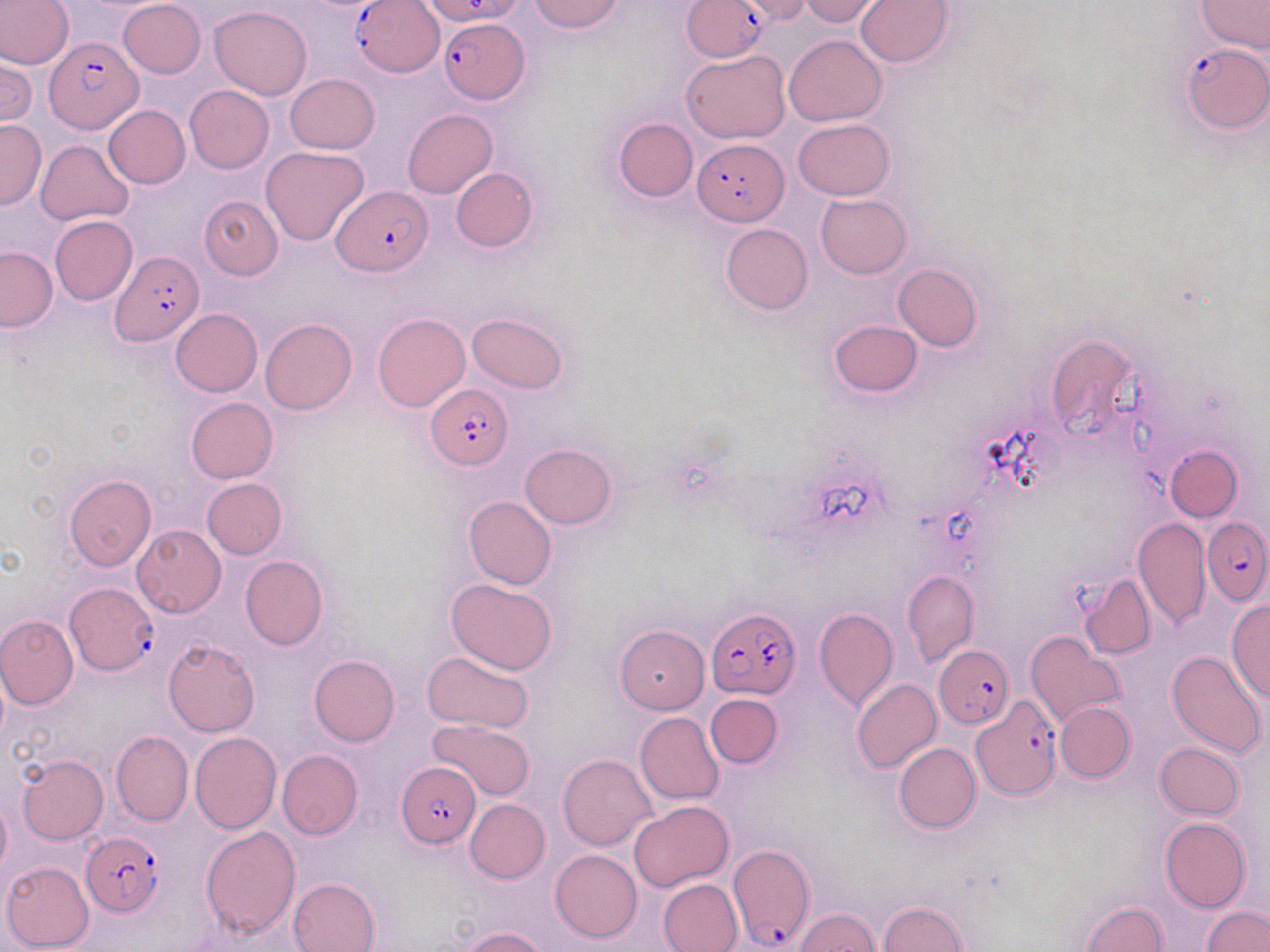
Summary:
  - Coordinate format: approximate bounding boxes as [x1, y1, x2, y2] in pixels
  - Uninfected red blood cell locations: [0, 0, 74, 70], [528, 0, 626, 34], [733, 0, 813, 23], [800, 0, 881, 25], [1196, 0, 1270, 55], [118, 1, 206, 79], [856, 1, 954, 68], [209, 6, 312, 100], [784, 35, 886, 126], [1, 50, 36, 129], [682, 50, 792, 144], [284, 74, 379, 154], [185, 85, 274, 174], [104, 105, 190, 189], [402, 109, 497, 198], [613, 117, 697, 201], [792, 118, 895, 200], [0, 119, 45, 210], [35, 139, 135, 226], [260, 145, 370, 247], [451, 167, 537, 252], [815, 194, 911, 278], [200, 196, 283, 280], [49, 214, 139, 305], [720, 223, 812, 315], [0, 246, 58, 332], [894, 263, 983, 352], [171, 308, 263, 397], [373, 312, 470, 411], [467, 312, 569, 393], [260, 318, 357, 415], [828, 320, 923, 398], [1043, 332, 1143, 442], [185, 397, 279, 483], [520, 443, 616, 529], [1165, 444, 1243, 521], [65, 475, 157, 570], [200, 478, 287, 560], [463, 495, 556, 590], [1133, 516, 1210, 631], [133, 524, 226, 618], [240, 555, 329, 649], [902, 570, 979, 666], [1079, 573, 1157, 659], [446, 578, 558, 675], [1226, 601, 1270, 703], [813, 607, 898, 711], [0, 615, 79, 709], [615, 624, 711, 714], [1024, 633, 1124, 729], [163, 638, 259, 735], [1167, 649, 1267, 758], [422, 650, 536, 736], [309, 654, 400, 747], [851, 678, 942, 773], [706, 693, 782, 767], [1055, 700, 1134, 783], [635, 712, 725, 804], [428, 719, 537, 801], [112, 730, 193, 826], [190, 732, 281, 833], [893, 742, 982, 833], [1154, 743, 1245, 820], [277, 749, 363, 840], [17, 753, 108, 844], [558, 753, 657, 852], [0, 796, 11, 879], [464, 799, 550, 883], [629, 800, 732, 891], [1160, 817, 1251, 913], [199, 824, 300, 938], [550, 850, 643, 942], [2, 861, 95, 950], [287, 877, 381, 952], [658, 878, 744, 952], [878, 901, 968, 952], [1080, 902, 1167, 952], [1201, 906, 1270, 952], [794, 908, 878, 951], [457, 926, 549, 952]
  - Plasmodium falciparum-infected red blood cell locations: [681, 0, 770, 61], [355, 1, 443, 77], [440, 16, 529, 103], [44, 37, 143, 134], [1179, 44, 1269, 132], [694, 137, 787, 226], [332, 184, 432, 276], [110, 250, 204, 345], [425, 385, 514, 468], [1202, 516, 1270, 601], [65, 581, 158, 675], [707, 607, 801, 700], [933, 645, 1012, 726], [966, 695, 1062, 798], [396, 763, 479, 847], [81, 832, 165, 918], [727, 843, 815, 950]
  - Slide-level diagnosis: Plasmodium falciparum
  - Stain: May-Grünwald-Giemsa
  - Image size: 1270×952 pixels
  - Preparation: thin blood film
  - Field of view: one of a larger specimen
  - Magnification: 1000x
  - Modality: light microscopy